Find the cells and give the type of each one.
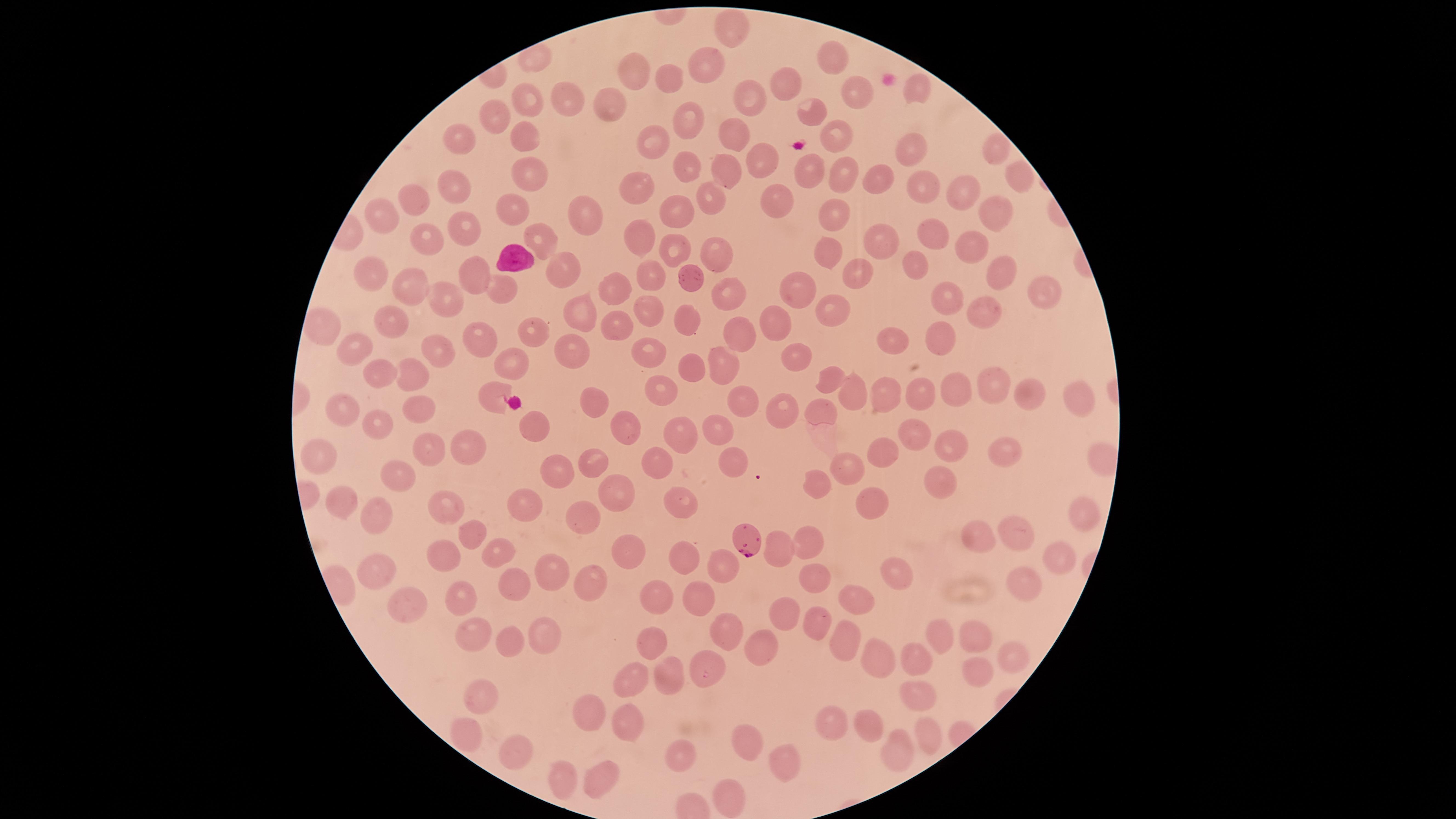
Approximate marker points as [x, y] in pixels.
Parasitized red blood cells: [746, 537].
Uninfected red blood cells: [731, 30], [832, 53], [699, 63], [632, 66], [788, 79], [665, 82], [916, 87], [850, 89], [743, 94], [610, 98], [564, 99], [530, 100], [805, 107], [501, 113], [685, 116], [836, 127], [730, 131], [461, 133], [526, 135], [655, 136], [908, 145], [991, 150], [767, 159], [690, 161], [529, 167], [735, 169], [811, 170], [848, 173], [1010, 173], [451, 181], [879, 181], [920, 184], [638, 188], [710, 193], [962, 193], [767, 195], [416, 199], [679, 204], [512, 207], [832, 210], [992, 211], [583, 216], [381, 218], [463, 223], [927, 233], [639, 237], [540, 239], [880, 239], [970, 239], [426, 243], [827, 244], [677, 250], [719, 252], [913, 259], [994, 266], [476, 267], [562, 270], [647, 272], [851, 274], [375, 275], [688, 276], [412, 286], [616, 286], [1033, 288], [499, 289], [798, 289], [722, 290], [449, 299], [950, 299], [647, 309], [579, 310], [830, 311], [985, 313], [686, 316], [773, 319], [394, 322], [615, 325], [743, 330], [535, 333], [939, 333], [893, 336], [480, 337], [439, 347], [573, 351], [649, 351], [516, 354], [348, 355], [795, 358], [726, 361], [698, 367], [413, 373], [384, 374], [826, 376], [992, 379], [856, 388], [1033, 388], [495, 390], [664, 390], [952, 390], [919, 393], [1068, 393], [741, 395], [883, 396], [593, 400], [342, 406], [418, 406], [783, 408], [823, 410], [377, 420], [630, 423], [534, 425], [715, 428], [682, 430], [917, 430], [951, 444], [467, 445], [428, 449], [318, 450], [878, 451], [1001, 455], [591, 459], [654, 459], [730, 459], [554, 468], [850, 468], [398, 474], [814, 480], [940, 480], [618, 490], [342, 499], [681, 499], [524, 501], [449, 505], [873, 506], [584, 514], [1079, 514], [376, 519], [1021, 527], [474, 531], [983, 533], [809, 540], [496, 545], [779, 546], [623, 548], [448, 551], [686, 551], [1053, 557], [379, 568], [719, 570], [551, 573], [814, 575], [897, 578], [591, 583], [519, 585], [1023, 589], [654, 593], [858, 593], [460, 594], [698, 595], [405, 608], [784, 618], [814, 619], [477, 632], [978, 632], [548, 635], [725, 636], [845, 637], [938, 637], [511, 638], [653, 646], [762, 649], [1010, 658], [875, 661], [912, 661], [707, 666], [971, 669], [669, 672], [635, 675], [480, 688], [916, 697], [587, 702], [631, 720], [871, 726], [926, 729], [828, 730], [461, 733], [749, 746], [897, 747], [514, 752], [676, 758], [781, 765], [561, 771], [602, 774], [726, 800].
White blood cells: [514, 257].

Summary:
  - Image size: 1456×819 pixels
  - Stain: Giemsa
  - Preparation: thin smear of blood
  - Species: Plasmodium falciparum
  - Field of view: single
  - Capture: smartphone photograph through the microscope eyepiece
  - Visible region: circular